Assess this cell for malaria.
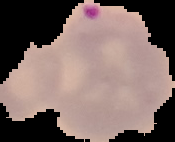

Parasitized.

From a thin blood smear. Segmented cell region on a black background. Image is 175×142 pixels.